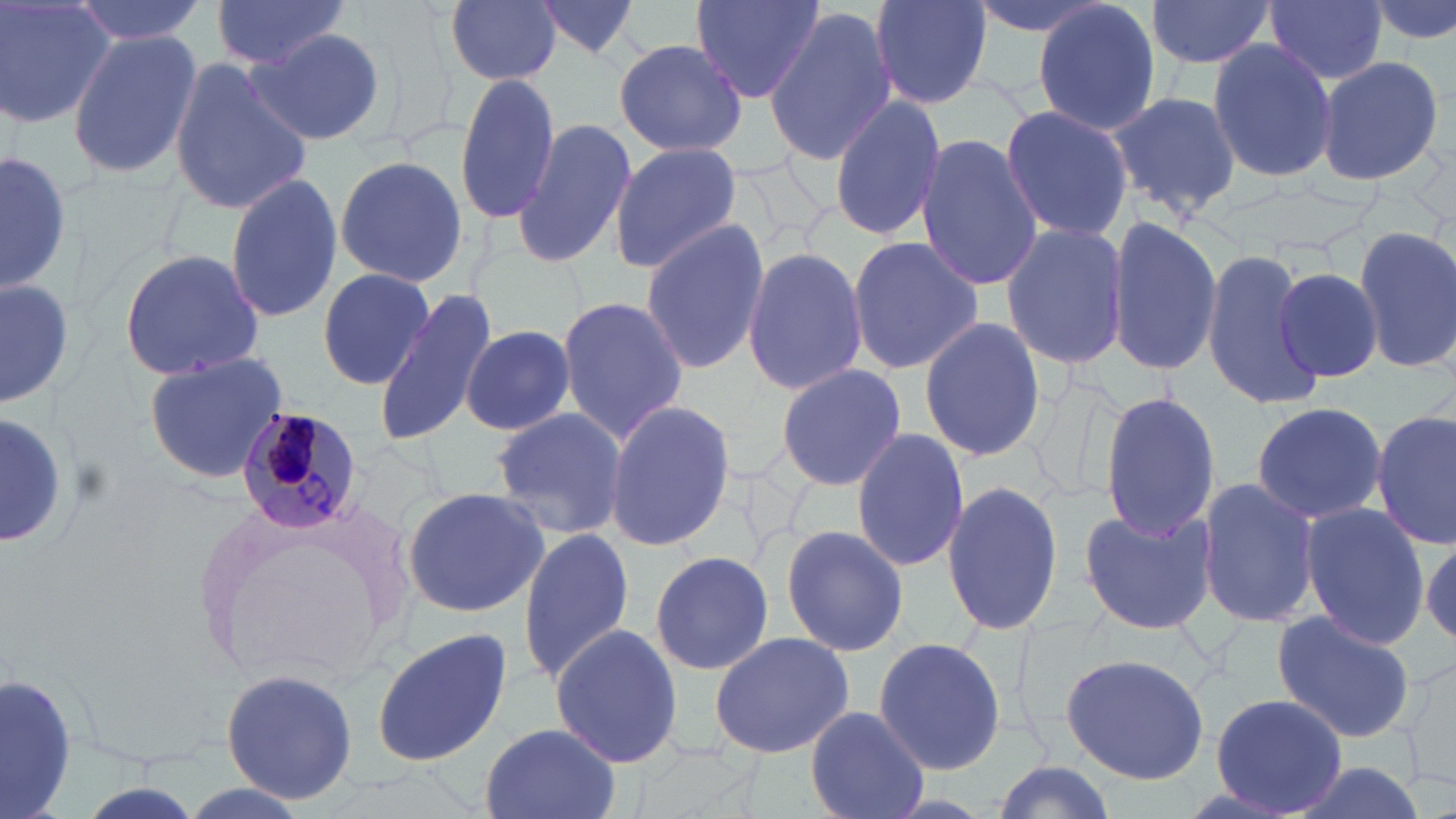
slide-level diagnosis = Plasmodium malariae
stain = May-Grünwald-Giemsa
Plasmodium malariae-infected red blood cell locations = approximate bounding boxes as [x1, y1, x2, y2] in pixels: [231, 406, 367, 538]
magnification = 1000x
field of view = single
preparation = thin blood film
image size = 1456×819 pixels
uninfected red blood cell locations = approximate bounding boxes as [x1, y1, x2, y2] in pixels: [1, 0, 113, 131], [73, 0, 208, 45], [209, 0, 352, 73], [445, 0, 562, 86], [532, 0, 646, 61], [690, 0, 824, 102], [870, 0, 995, 109], [968, 0, 1113, 39], [1369, 0, 1456, 50], [1030, 1, 1163, 138], [1148, 2, 1275, 73], [1265, 3, 1389, 86], [764, 6, 896, 168], [244, 27, 386, 148], [67, 30, 200, 180], [614, 37, 747, 159], [1205, 37, 1337, 187], [1316, 53, 1446, 186], [168, 57, 313, 216], [453, 69, 559, 225], [1104, 89, 1242, 217], [828, 93, 947, 242], [998, 104, 1135, 243], [514, 117, 638, 270], [914, 134, 1042, 290], [608, 141, 744, 277], [0, 150, 71, 296], [333, 155, 468, 286], [222, 173, 343, 321], [1105, 216, 1224, 378], [640, 220, 771, 374], [999, 222, 1130, 371], [1352, 224, 1456, 376], [846, 236, 985, 375], [741, 245, 868, 397], [117, 247, 265, 382], [1200, 248, 1322, 410], [1271, 264, 1386, 385], [317, 266, 436, 391], [0, 275, 76, 412], [372, 288, 501, 445], [556, 295, 689, 445], [916, 312, 1044, 466], [460, 325, 577, 436], [145, 351, 291, 486], [774, 362, 908, 492], [1098, 390, 1223, 540], [603, 400, 735, 551], [1249, 401, 1388, 524], [488, 408, 628, 540], [1373, 410, 1456, 551], [0, 412, 69, 547], [852, 425, 971, 575], [1198, 477, 1321, 630], [941, 478, 1064, 639], [403, 484, 551, 619], [1078, 503, 1216, 637], [1299, 503, 1429, 649], [780, 524, 909, 658], [516, 530, 634, 682], [1421, 535, 1456, 652], [650, 550, 773, 677], [1271, 610, 1418, 743], [551, 624, 684, 769], [369, 629, 513, 768], [707, 631, 854, 758], [870, 635, 1007, 777], [1060, 654, 1209, 785], [218, 668, 361, 805], [0, 676, 81, 819], [1208, 694, 1351, 816], [806, 705, 928, 819], [478, 722, 623, 819], [1282, 760, 1430, 819], [987, 761, 1121, 819]
modality = optical microscopy